Locate every malaria parasite.
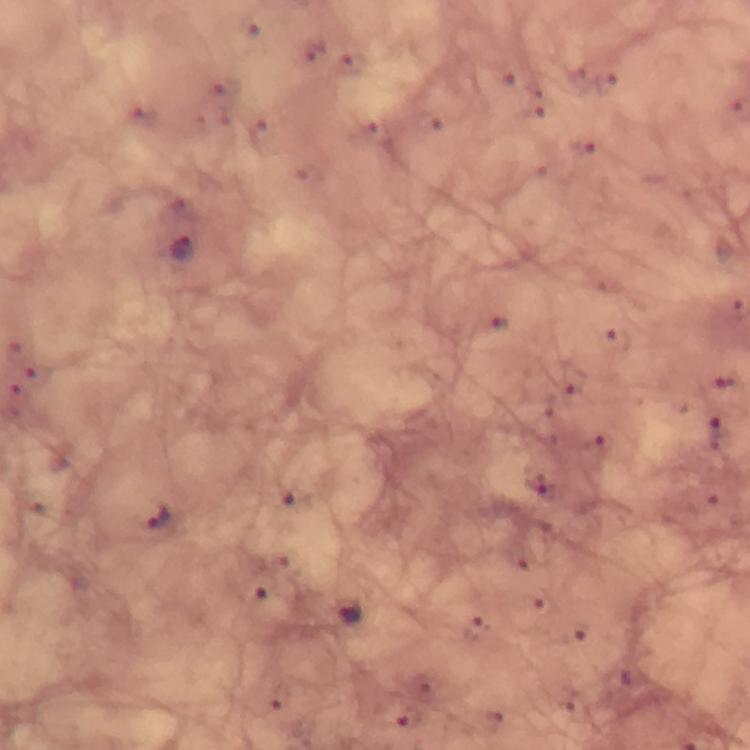
Approximate centers as {x, y} in pixels.
Malaria parasites: {180, 249}, {157, 518}, {348, 614}.

Summary:
  - Magnification: 100x
  - Context: from a diagnostic examination for malaria
  - Stain: Giemsa
  - Capture: smartphone camera through the microscope
  - Preparation: thick blood film
  - Immersion oil: applied
  - Image size: 750×750 pixels
  - Cropped from: one field of view